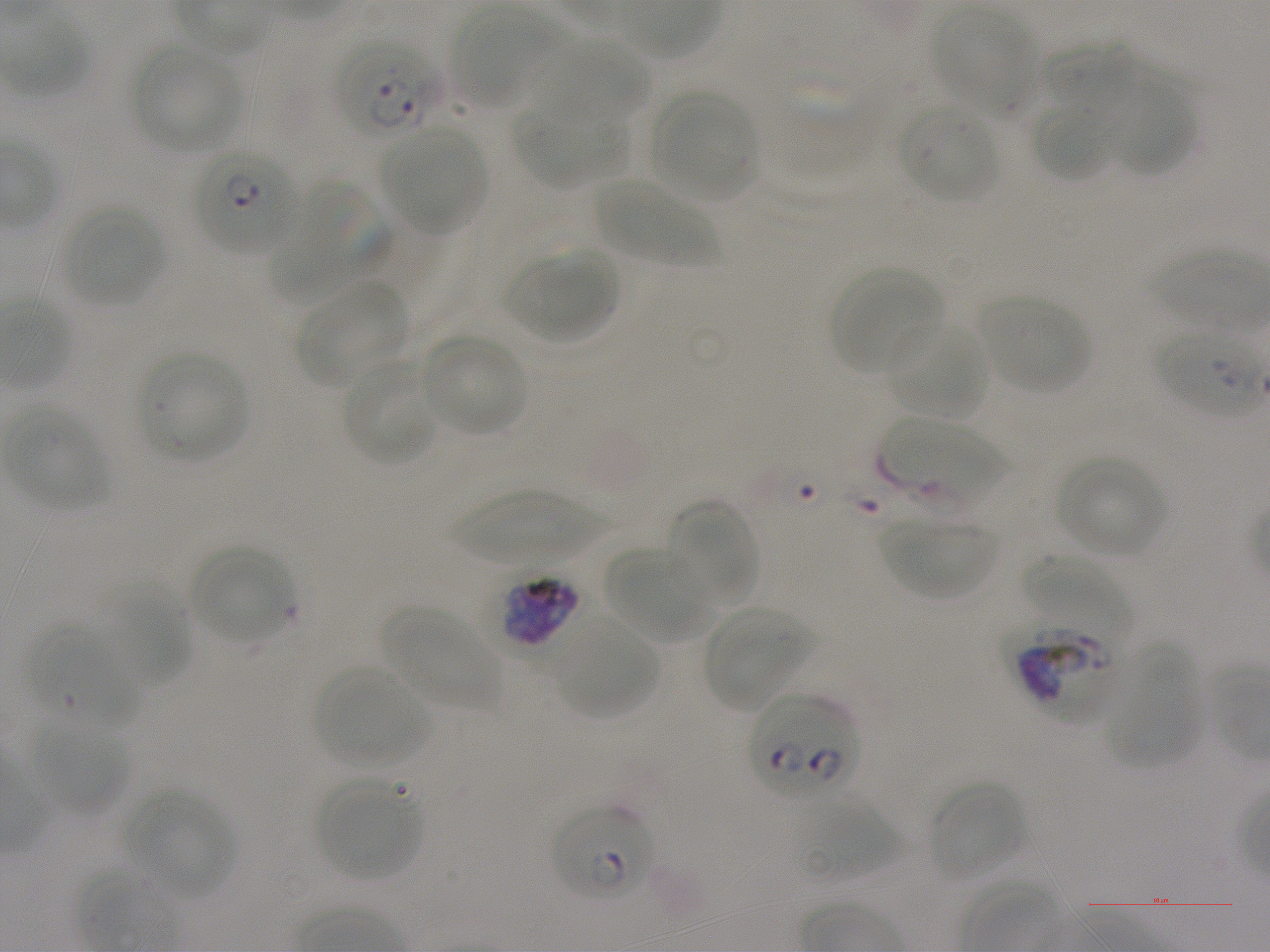

Approximate bounding boxes as (x1, y1, x2, y2) in pixels. Not every red blood cell is marked. A life-cycle stage — or a range of stages, where the recorded stages span more than one — follows each staged infected red blood cell.
Summary:
  - Locations of infected red blood cells: (194, 147, 298, 256) ring; (1155, 326, 1270, 416) ring; (500, 574, 582, 649) late trophozoite to late schizont; (749, 695, 861, 804); (550, 804, 656, 904) ring
  - Locations of uninfected red blood cells: (451, 6, 570, 111), (932, 9, 1041, 119), (538, 39, 648, 123), (1043, 39, 1135, 111), (133, 45, 244, 154), (1102, 73, 1196, 176), (650, 91, 760, 202), (513, 97, 624, 189), (1030, 101, 1116, 183), (900, 103, 998, 203), (380, 126, 486, 234), (593, 178, 716, 267), (273, 179, 392, 298), (64, 205, 164, 306), (506, 250, 614, 343), (829, 267, 944, 376), (297, 284, 407, 388), (977, 294, 1092, 394), (885, 322, 987, 419), (420, 334, 529, 436), (138, 353, 250, 463), (340, 357, 439, 467), (6, 404, 111, 510), (883, 418, 1015, 517), (1056, 454, 1167, 558), (447, 489, 607, 563), (663, 499, 762, 609), (879, 517, 998, 600), (189, 545, 296, 644), (605, 546, 717, 644), (1022, 555, 1130, 636), (100, 586, 190, 689), (383, 607, 500, 712), (703, 607, 812, 712), (556, 618, 656, 718), (1108, 645, 1203, 768), (315, 665, 430, 770), (31, 722, 129, 815), (317, 776, 425, 881), (927, 779, 1027, 883), (125, 790, 234, 899), (796, 797, 923, 883)
  - Locations of red blood cells of indeterminate infection status: (336, 39, 444, 139), (1001, 618, 1122, 724), (27, 624, 137, 732)
  - Image size: 1270×952 pixels
  - Culture: in-vitro P. falciparum strain NF54, static
  - Objective: 100x, oil immersion, numerical aperture 1.25
  - Donor blood group: A+
  - Stain: Giemsa
  - Field of view: single
  - Preparation: thin blood film